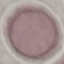 Malaria status: uninfected. Thin smear of blood. Giemsa stain. Cell patch, automatically extracted from a larger field of view and resized to 64 × 64 pixels. Photographed with a smartphone camera at the microscope eyepiece.